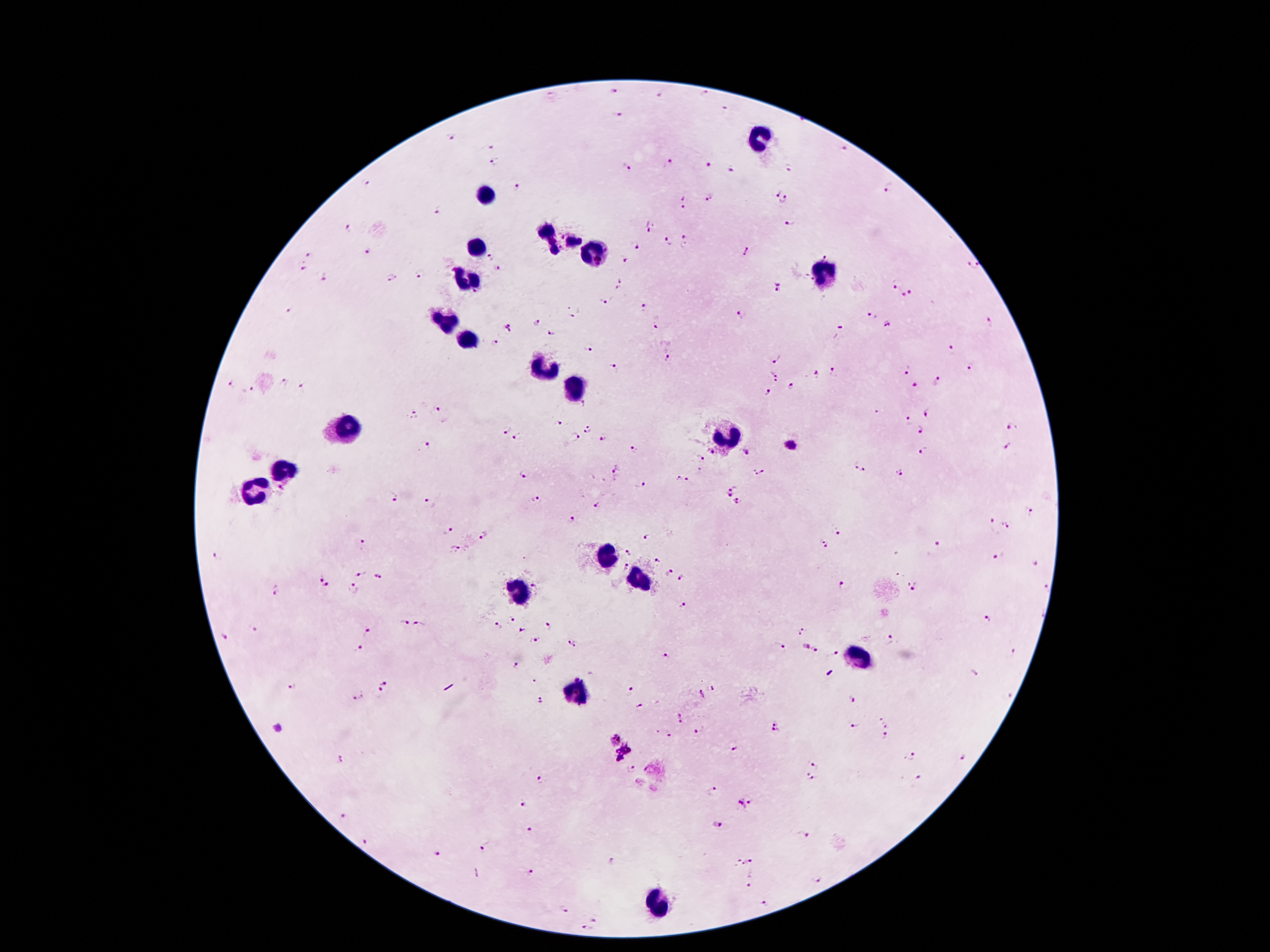
Approximate object centers, in pixels from the top-left corner. Plasmodium parasite locations: (x=613, y=91), (x=707, y=95), (x=660, y=96), (x=725, y=110), (x=617, y=116), (x=452, y=138), (x=490, y=146), (x=842, y=148), (x=496, y=163), (x=671, y=164), (x=711, y=164), (x=627, y=169), (x=732, y=169), (x=789, y=169), (x=369, y=183), (x=519, y=186), (x=888, y=187), (x=776, y=194), (x=685, y=199), (x=710, y=199), (x=785, y=201), (x=439, y=209), (x=790, y=224), (x=651, y=226), (x=348, y=229), (x=685, y=240), (x=667, y=241), (x=635, y=244), (x=746, y=250), (x=367, y=253), (x=308, y=255), (x=824, y=255), (x=490, y=256), (x=625, y=258), (x=972, y=265), (x=303, y=268), (x=497, y=269), (x=420, y=275), (x=393, y=278), (x=323, y=280), (x=897, y=282), (x=619, y=284), (x=775, y=288), (x=911, y=293), (x=903, y=295), (x=605, y=302), (x=643, y=307), (x=287, y=309), (x=574, y=315), (x=742, y=316), (x=873, y=316), (x=536, y=322), (x=990, y=322), (x=888, y=325), (x=507, y=328), (x=653, y=328), (x=838, y=332), (x=550, y=335), (x=497, y=342), (x=590, y=349), (x=950, y=349), (x=667, y=358), (x=777, y=359), (x=971, y=367), (x=612, y=369), (x=906, y=371), (x=834, y=372), (x=776, y=375), (x=817, y=375), (x=937, y=381), (x=230, y=383), (x=284, y=383), (x=915, y=386), (x=304, y=387), (x=792, y=387), (x=247, y=390), (x=769, y=394), (x=438, y=410), (x=878, y=411), (x=928, y=412), (x=413, y=414), (x=559, y=422), (x=907, y=422), (x=1009, y=426), (x=588, y=429), (x=506, y=430), (x=918, y=430), (x=574, y=437), (x=516, y=438), (x=603, y=439), (x=791, y=444), (x=427, y=445), (x=636, y=449), (x=924, y=449), (x=1008, y=449), (x=714, y=452), (x=745, y=452), (x=701, y=458), (x=855, y=467), (x=864, y=470), (x=615, y=471), (x=761, y=472), (x=901, y=473), (x=524, y=474), (x=678, y=478), (x=688, y=480), (x=639, y=485), (x=283, y=488), (x=733, y=488), (x=728, y=495), (x=393, y=497), (x=535, y=499), (x=738, y=502), (x=429, y=503), (x=597, y=506), (x=1029, y=511), (x=571, y=519), (x=990, y=520), (x=1004, y=526), (x=838, y=530), (x=449, y=532), (x=486, y=535), (x=649, y=536), (x=936, y=543), (x=363, y=544), (x=824, y=544), (x=453, y=549), (x=629, y=553), (x=216, y=555), (x=998, y=557), (x=659, y=559), (x=1034, y=563), (x=624, y=566), (x=669, y=573), (x=358, y=574), (x=320, y=578), (x=377, y=578), (x=681, y=579), (x=841, y=585), (x=536, y=586), (x=329, y=587), (x=353, y=589), (x=279, y=591), (x=914, y=591), (x=684, y=605), (x=988, y=618), (x=512, y=620), (x=404, y=621), (x=418, y=624), (x=498, y=625), (x=547, y=626), (x=254, y=629), (x=521, y=630), (x=368, y=631), (x=804, y=631), (x=223, y=637), (x=890, y=639), (x=536, y=641), (x=572, y=643), (x=779, y=645), (x=805, y=645), (x=360, y=646), (x=816, y=650), (x=1012, y=652), (x=836, y=653), (x=664, y=656), (x=516, y=666), (x=972, y=671), (x=535, y=681), (x=383, y=682), (x=292, y=688), (x=713, y=688), (x=630, y=691), (x=380, y=692), (x=702, y=694), (x=357, y=696), (x=852, y=700), (x=541, y=702), (x=641, y=708), (x=680, y=717), (x=880, y=719), (x=774, y=720), (x=856, y=726), (x=278, y=727), (x=887, y=727), (x=776, y=731), (x=699, y=732), (x=668, y=735), (x=886, y=737), (x=615, y=740), (x=626, y=748), (x=733, y=749), (x=914, y=756), (x=963, y=758), (x=617, y=759), (x=339, y=760), (x=815, y=765), (x=632, y=769), (x=810, y=777), (x=917, y=777), (x=538, y=780), (x=714, y=790), (x=524, y=804), (x=746, y=804), (x=344, y=817), (x=717, y=825), (x=530, y=832), (x=804, y=836), (x=363, y=845), (x=483, y=848), (x=443, y=854), (x=610, y=861), (x=750, y=861), (x=475, y=871), (x=531, y=872), (x=817, y=880), (x=748, y=887), (x=765, y=903), (x=566, y=907), (x=595, y=922), (x=584, y=928). Leukocyte locations: (x=759, y=136), (x=488, y=196), (x=558, y=241), (x=475, y=247), (x=596, y=254), (x=821, y=274), (x=467, y=282), (x=445, y=323), (x=467, y=341), (x=537, y=368), (x=574, y=385), (x=348, y=428), (x=729, y=433), (x=285, y=469), (x=258, y=488), (x=606, y=556), (x=638, y=579), (x=518, y=590), (x=857, y=659), (x=579, y=695), (x=660, y=904). Thick peripheral-blood smear. Image is 1270×952 pixels. One field from this slide. Photographed through the microscope eyepiece with a smartphone camera. Giemsa stain. 100x magnification. Patient malaria status: positive for Plasmodium falciparum.